State the blood parasite species.
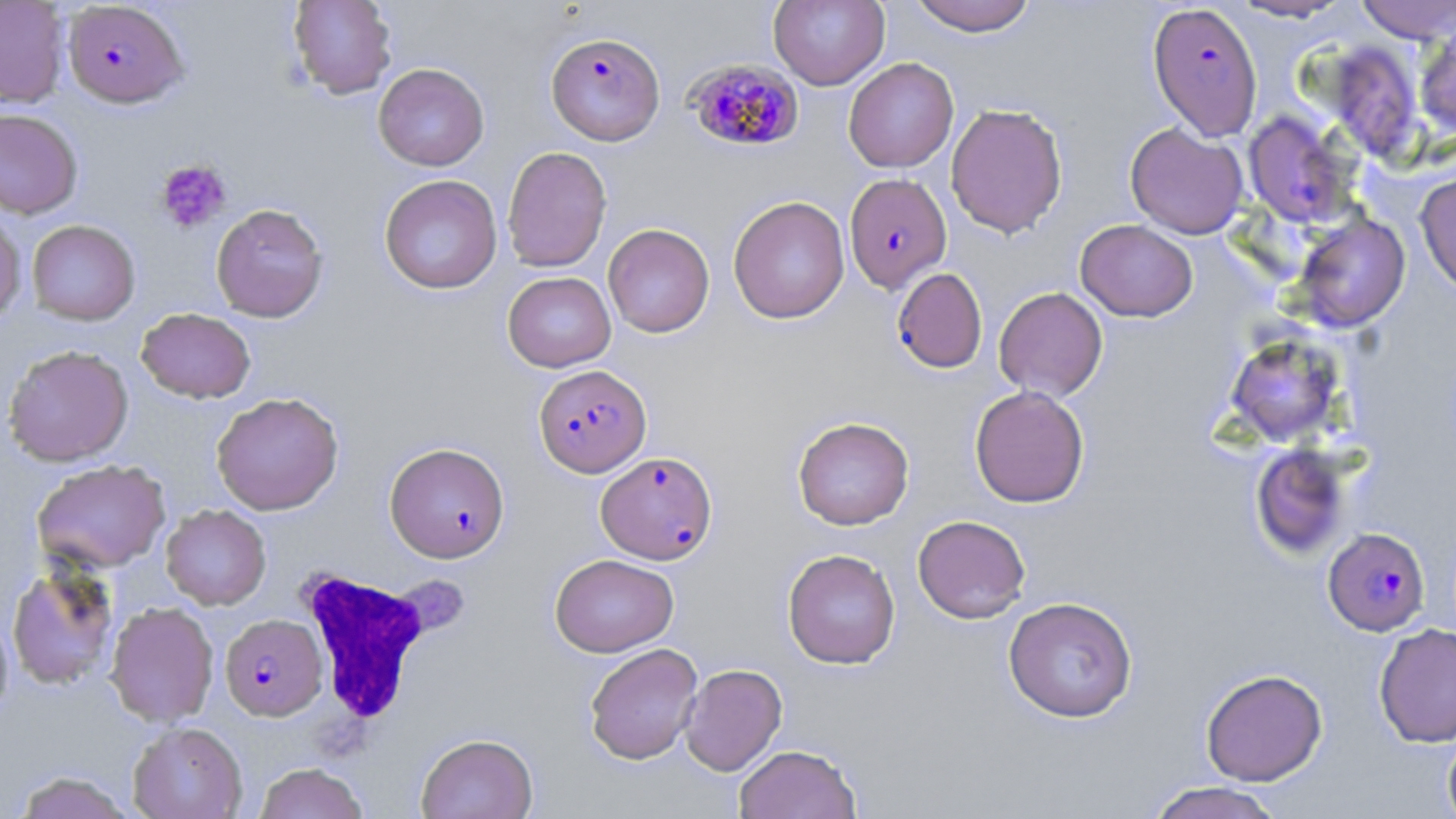
Plasmodium falciparum.

Summary:
  - Coordinate format: approximate bounding boxes as [x1, y1, x2, y2] in pixels
  - Uninfected red blood cell locations: [288, 0, 398, 99], [769, 0, 889, 90], [908, 0, 1037, 36], [1227, 0, 1354, 22], [1355, 0, 1456, 43], [0, 1, 69, 108], [1415, 24, 1456, 137], [1325, 40, 1423, 162], [843, 57, 959, 172], [373, 63, 489, 171], [945, 103, 1068, 238], [0, 108, 83, 219], [1242, 111, 1358, 229], [1125, 123, 1249, 239], [501, 146, 612, 272], [1415, 170, 1456, 296], [379, 174, 502, 294], [728, 195, 850, 324], [211, 203, 328, 322], [0, 206, 26, 327], [1292, 212, 1410, 332], [1075, 219, 1198, 322], [27, 220, 140, 325], [603, 223, 715, 338], [502, 271, 616, 372], [994, 286, 1108, 402], [136, 308, 256, 403], [1225, 333, 1345, 446], [3, 344, 134, 467], [969, 385, 1090, 508], [211, 392, 344, 515], [792, 416, 914, 530], [1250, 443, 1352, 559], [33, 459, 171, 572], [161, 505, 271, 610], [913, 514, 1031, 623], [782, 548, 901, 669], [550, 553, 678, 657], [6, 561, 121, 692], [1003, 597, 1138, 723], [105, 601, 219, 727], [0, 605, 14, 726], [1374, 623, 1456, 748], [584, 642, 703, 765], [679, 663, 787, 776], [1201, 668, 1327, 786], [127, 722, 247, 819], [1442, 728, 1456, 819], [416, 732, 538, 819], [734, 744, 862, 819], [255, 763, 368, 819], [13, 771, 136, 818], [1146, 781, 1286, 819]
  - Platelet locations: [155, 160, 232, 233]
  - White blood cell locations: [296, 565, 438, 729]
  - Plasmodium falciparum-infected red blood cell locations: [62, 1, 189, 108], [1147, 2, 1262, 140], [545, 31, 665, 146], [686, 58, 804, 152], [845, 175, 953, 294], [892, 268, 987, 373], [533, 364, 651, 478], [385, 442, 510, 562], [596, 450, 717, 564], [1324, 527, 1430, 636], [220, 614, 327, 720]
  - Field of view: one of a larger specimen
  - Image size: 1456×819 pixels
  - Preparation: thin blood film
  - Magnification: 1000x
  - Modality: light microscopy
  - Stain: May-Grünwald-Giemsa